Give the extent of all uninfected red blood cells.
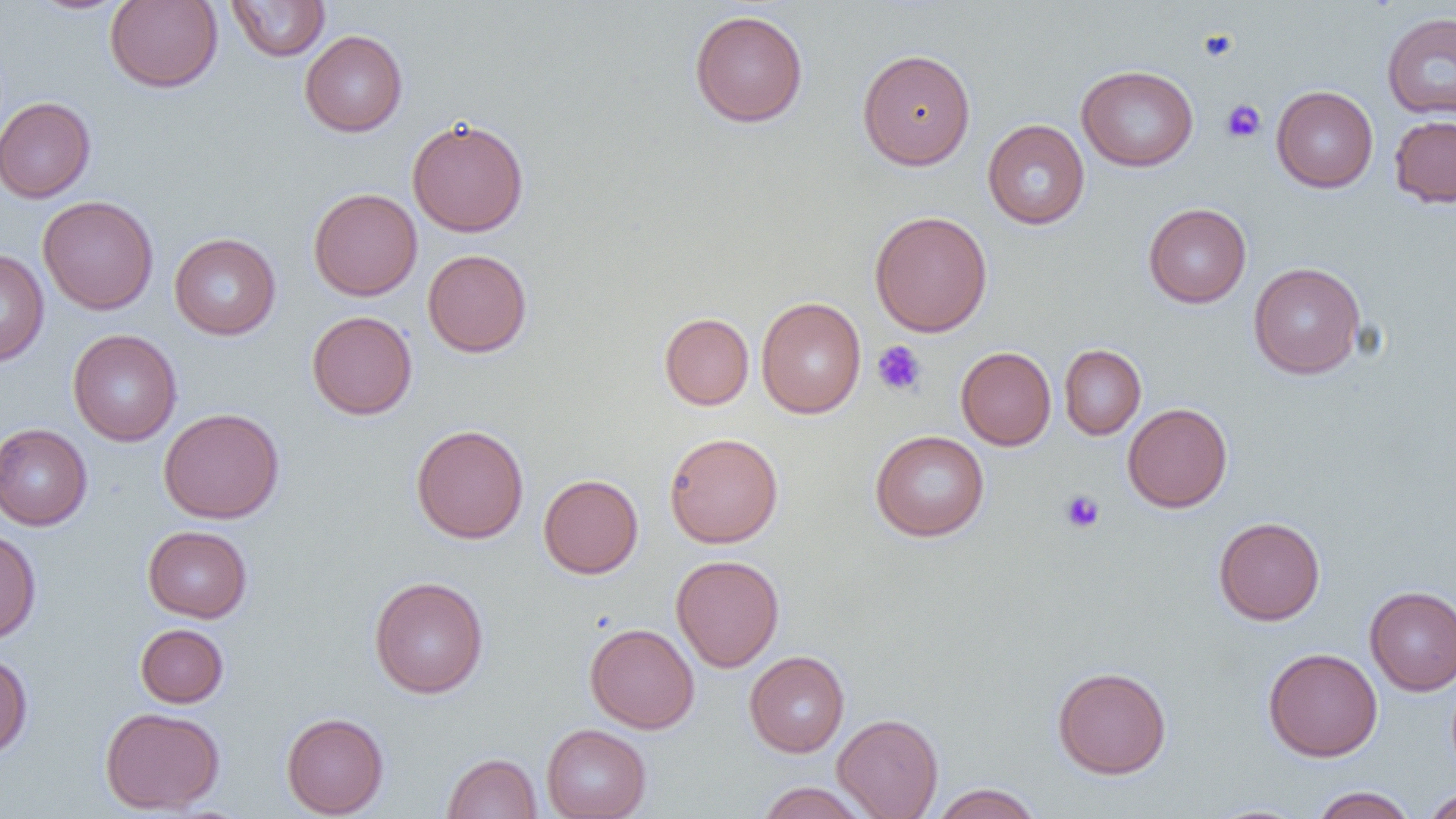

Approximate bounding boxes as (x1,y1)-(x2,y2) corner pairs in pixels.
Uninfected red blood cells: (26,0)-(134,15), (105,0)-(223,92), (227,1)-(330,61), (689,9)-(808,127), (1382,12)-(1456,119), (300,30)-(408,137), (858,48)-(976,170), (1077,65)-(1198,172), (1271,86)-(1378,193), (0,96)-(96,203), (1389,115)-(1456,208), (407,117)-(529,237), (983,119)-(1090,229), (308,188)-(422,301), (38,195)-(159,315), (1143,203)-(1251,308), (869,210)-(993,337), (169,233)-(281,340), (0,248)-(49,367), (422,249)-(532,358), (1248,262)-(1365,379), (755,296)-(866,419), (306,310)-(417,419), (659,312)-(754,410), (67,329)-(182,446), (1059,344)-(1146,439), (955,346)-(1056,450), (1122,403)-(1233,513), (158,407)-(285,523), (0,423)-(92,530), (411,424)-(529,544), (870,430)-(990,542), (664,432)-(783,548), (538,474)-(643,578), (1213,516)-(1325,625), (143,525)-(252,622), (0,528)-(41,644), (670,554)-(785,672), (369,576)-(489,698), (1365,586)-(1456,695), (135,623)-(228,707), (585,623)-(699,734), (1263,647)-(1383,761), (0,650)-(33,759), (744,651)-(849,757), (1052,666)-(1172,779), (100,707)-(225,814), (281,712)-(389,818), (832,713)-(943,819), (541,723)-(651,819), (442,752)-(542,818), (755,782)-(874,818), (929,783)-(1043,819), (1310,786)-(1417,818), (1421,788)-(1456,819).

Summary:
  - Platelet locations: (1198,28)-(1239,63), (1221,99)-(1266,143), (872,341)-(927,396), (1060,490)-(1105,533)
  - Slide-level diagnosis: negative for blood parasites
  - Modality: optical microscopy
  - Field of view: single
  - Magnification: 1000x
  - Preparation: thin blood smear
  - Image size: 1456×819 pixels